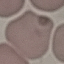
Summary:
  - Result: no malaria parasites detected
  - Capture: smartphone camera at the microscope eyepiece
  - Stain: Giemsa
  - Preparation: thin smear
  - Image type: cell patch, automatically extracted from a larger field of view and resized to 64 × 64 pixels